Identify the cell.
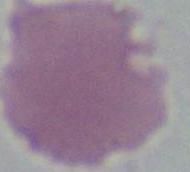
An erythrocyte.

Captured at 1000x magnification. Photomicrograph.